Identify the parasite.
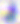

Toxoplasma gondii.

Summary:
  - Modality: micrograph
  - Magnification: 400x